Report the malaria status of this cell.
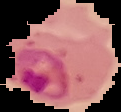

Parasitized.

Summary:
  - Image size: 121×112 pixels
  - Preparation: thin blood film
  - Image type: cell region segmented out of the field of view; surrounding area masked to black